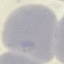

Result: no malaria parasites seen. Acquired by smartphone through the microscope eyepiece. Cell patch, automatically extracted from a larger field of view and resized to 64 × 64 pixels. Giemsa-stained preparation. Thin blood smear.